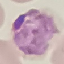
Summary:
  - Malaria status: parasitized
  - Capture: smartphone camera at the microscope eyepiece
  - Image type: cell patch, automatically extracted from a larger field of view and resized to 64 × 64 pixels
  - Preparation: thin blood smear
  - Stain: Giemsa